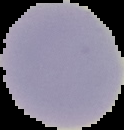
Segmented cell region on a black background. Malaria status: uninfected. From a thin blood film. Image is 124×130 pixels.